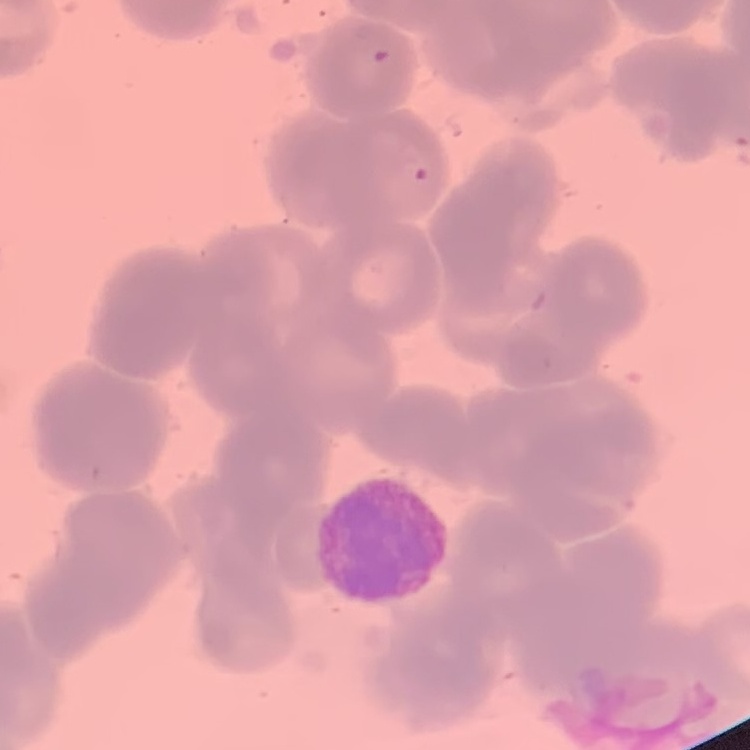

The red blood cells show rouleaux formation. Stained with either Field's or Giemsa. Thin blood film. One tile cut from a larger photomicrograph.